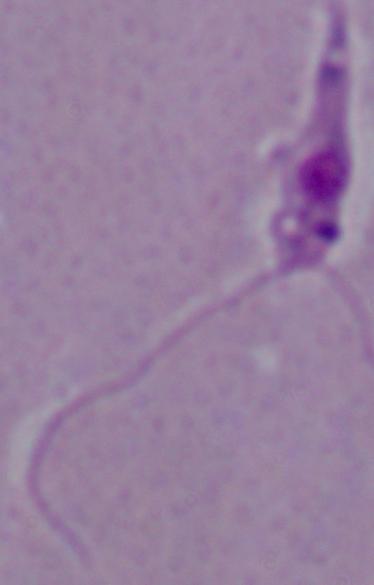
modality: photomicrograph
identification: Leishmania
magnification: 1000x